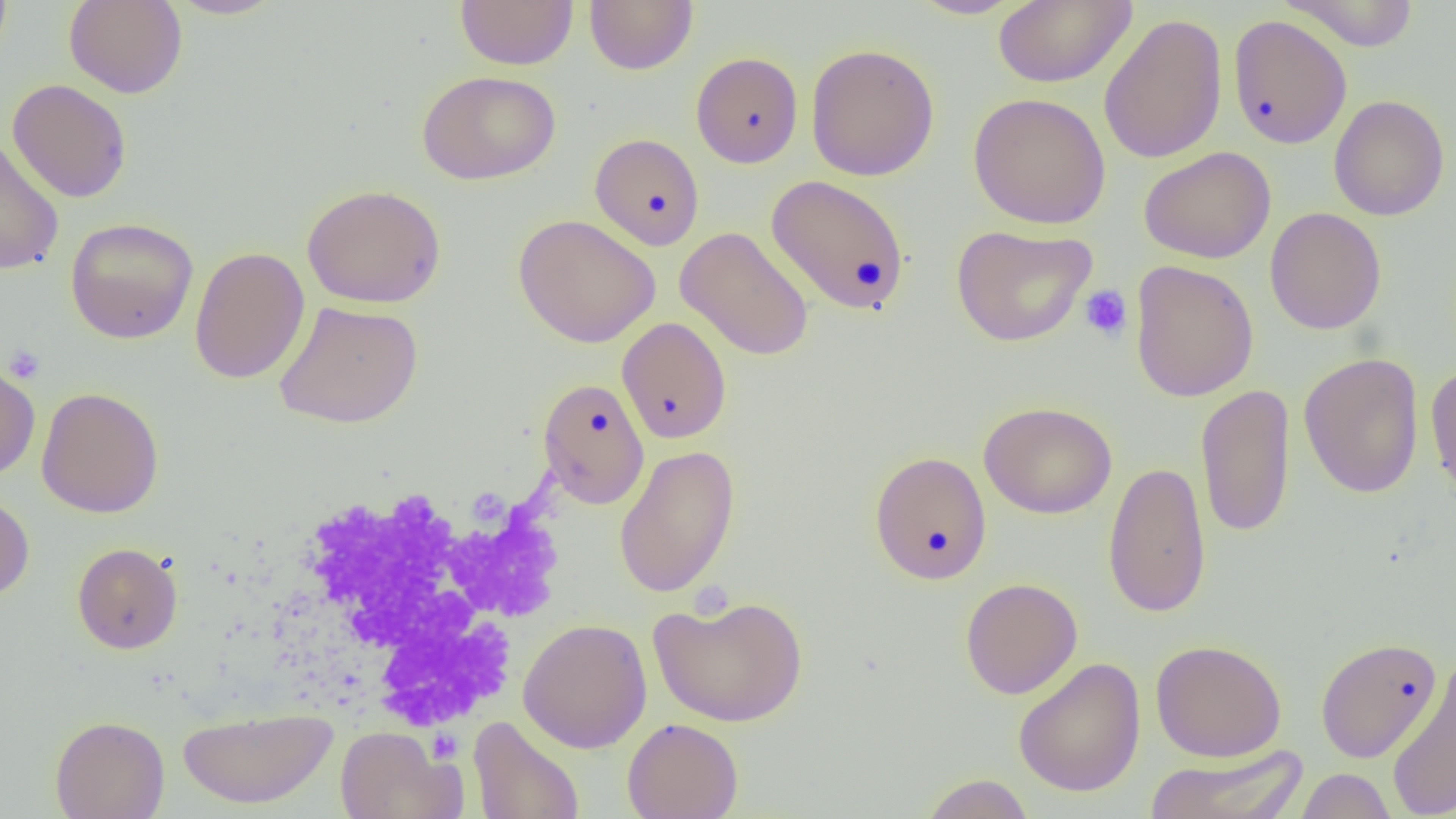
Summary:
  - Coordinate format: approximate bounding boxes as (x1, y1, x2, y2) in pixels
  - Uninfected red blood cell locations: (0, 0, 13, 67), (64, 0, 187, 98), (166, 0, 286, 19), (455, 0, 578, 69), (585, 0, 698, 75), (908, 0, 1027, 19), (993, 0, 1136, 87), (1280, 0, 1419, 51), (1098, 14, 1228, 164), (1228, 15, 1352, 149), (805, 43, 940, 181), (691, 51, 803, 168), (417, 70, 560, 185), (7, 79, 132, 203), (968, 92, 1111, 229), (1329, 94, 1450, 221), (590, 134, 704, 250), (0, 138, 64, 276), (1139, 146, 1276, 264), (766, 175, 911, 315), (302, 184, 446, 308), (1265, 207, 1386, 335), (512, 213, 661, 348), (65, 217, 199, 344), (950, 224, 1096, 347), (675, 226, 814, 361), (190, 247, 310, 384), (1130, 260, 1259, 402), (275, 300, 423, 429), (617, 317, 731, 443), (1299, 352, 1424, 498), (0, 362, 40, 482), (1424, 363, 1456, 500), (537, 377, 650, 509), (1195, 383, 1295, 538), (36, 387, 165, 518), (979, 401, 1117, 519), (614, 445, 740, 598), (869, 451, 992, 584), (1103, 461, 1212, 618), (0, 491, 35, 602), (72, 542, 183, 653), (960, 577, 1082, 699), (648, 594, 809, 727), (518, 618, 652, 753), (1315, 636, 1443, 763), (1150, 639, 1287, 762), (1012, 657, 1146, 797), (1386, 658, 1456, 819), (177, 706, 338, 809), (50, 715, 169, 819), (468, 715, 584, 819), (622, 717, 743, 819), (335, 725, 460, 818), (1143, 743, 1309, 819), (1295, 767, 1397, 818), (920, 774, 1034, 819)
  - Platelet locations: (1079, 284, 1133, 342), (3, 344, 46, 384)
  - White blood cell locations: (269, 485, 558, 734)
  - Slide-level diagnosis: no evidence of blood parasites
  - Field of view: single
  - Preparation: thin blood smear
  - Image size: 1456×819 pixels
  - Modality: optical microscopy
  - Magnification: 1000x